Assess this cell for malaria.
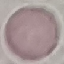
It is uninfected.

Summary:
  - Stain: Giemsa
  - Capture: smartphone camera at the microscope eyepiece
  - Image type: cell patch, automatically extracted from a larger field of view and resized to 64 × 64 pixels
  - Preparation: thin blood smear